Classify this cell by malaria status.
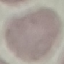
It is uninfected.

Summary:
  - Stain: Giemsa
  - Image type: cell patch, automatically extracted from a larger field of view and resized to 64 × 64 pixels
  - Preparation: thin blood smear
  - Capture: smartphone camera at the microscope eyepiece